Point out each Plasmodium parasite.
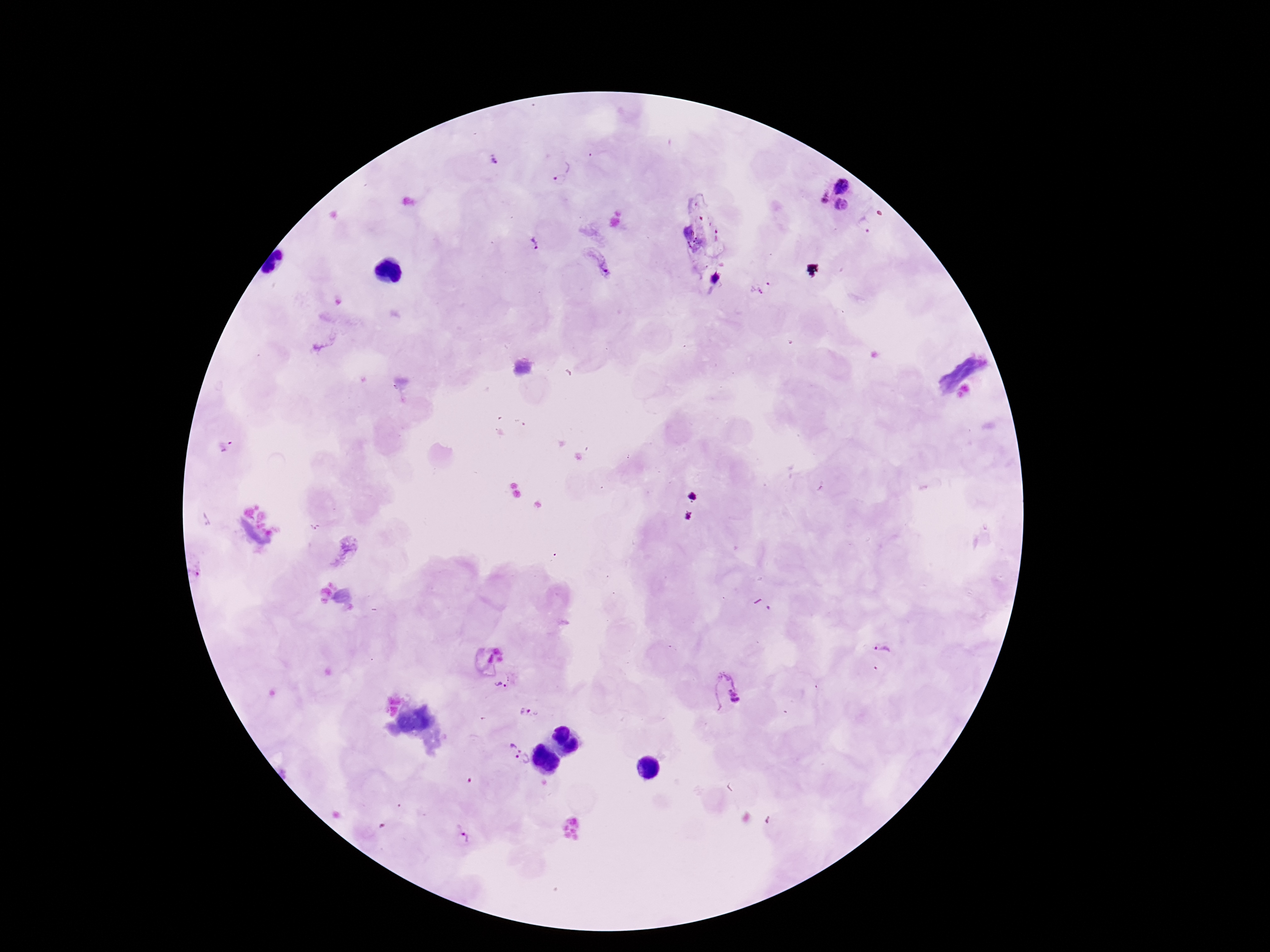

Approximate centers as [x, y] in pixels.
Plasmodium parasites: [495, 159], [559, 181], [843, 184], [822, 196], [842, 205], [534, 242], [597, 260], [225, 448], [198, 567], [883, 648], [502, 679], [725, 692], [530, 712], [514, 740], [524, 764], [461, 836].

Giemsa stain. Thick blood smear. One field from this slide. Patient malaria status: positive. Smartphone photograph taken through the microscope eyepiece. 100x magnification. Image is 1270×952 pixels.